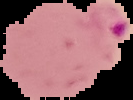

Summary:
  - Image size: 133×100 pixels
  - Image type: segmented cell region on a black background
  - Preparation: thin blood film
  - Result: Plasmodium parasites identified